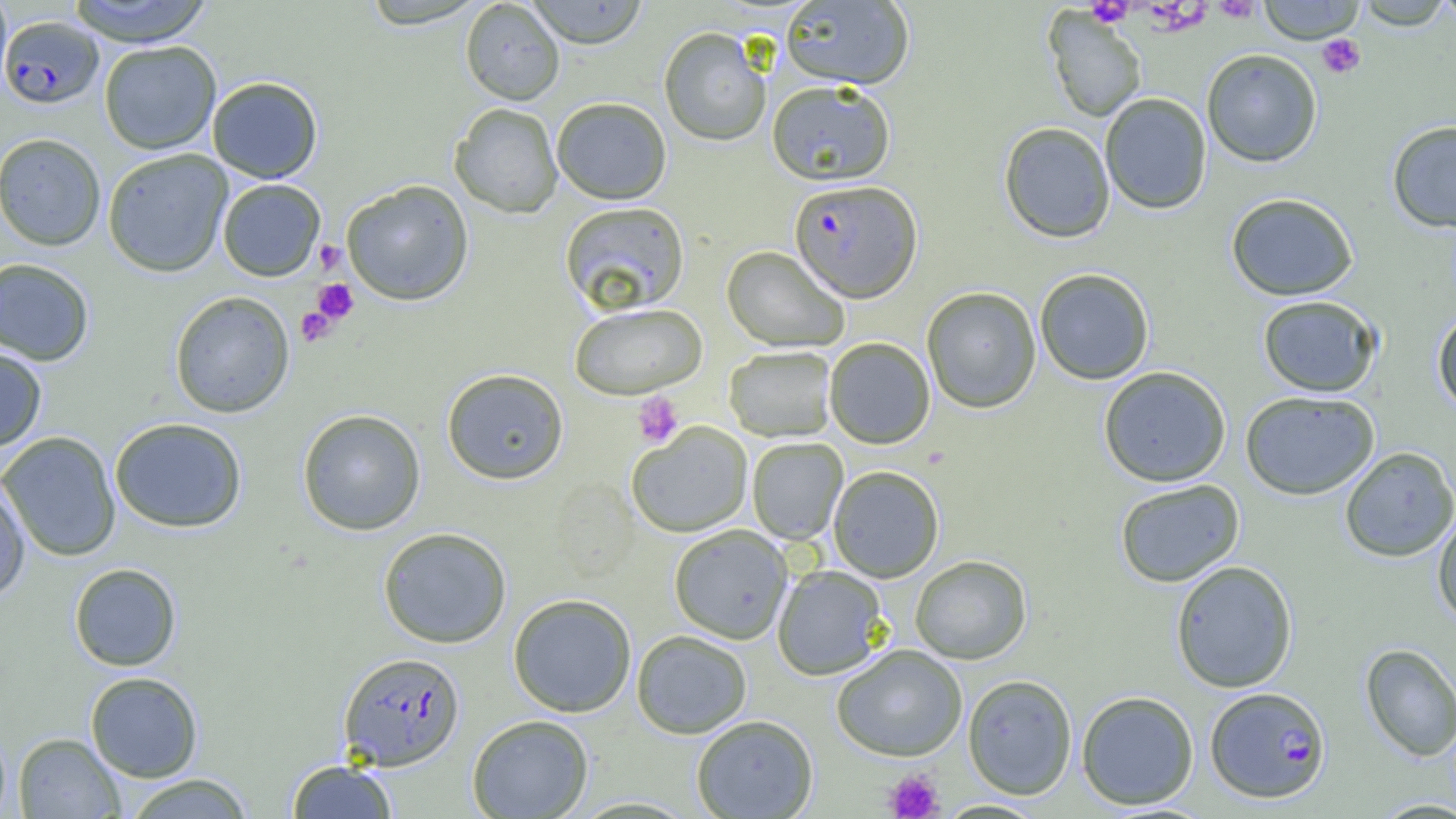

slide-level diagnosis = Plasmodium falciparum
platelet locations = approximate bounding boxes as [x1, y1, x2, y2] in pixels: [1211, 0, 1262, 23], [1086, 1, 1133, 27], [1317, 34, 1366, 78], [314, 240, 346, 274], [310, 279, 359, 326], [295, 305, 338, 347], [632, 392, 684, 448], [883, 768, 944, 818]
uninfected red blood cell locations = approximate bounding boxes as [x1, y1, x2, y2] in pixels: [0, 0, 13, 101], [64, 0, 216, 45], [357, 0, 489, 30], [460, 0, 565, 105], [526, 0, 649, 48], [1256, 0, 1366, 43], [1431, 0, 1456, 27], [781, 1, 914, 89], [1353, 2, 1456, 30], [1043, 10, 1147, 123], [659, 27, 771, 146], [99, 40, 222, 154], [1201, 49, 1323, 167], [207, 76, 323, 183], [766, 80, 896, 185], [1099, 93, 1212, 215], [551, 97, 672, 204], [449, 102, 564, 218], [1386, 120, 1456, 233], [998, 122, 1116, 243], [0, 132, 107, 251], [102, 149, 233, 277], [217, 179, 326, 281], [341, 179, 474, 306], [1225, 192, 1359, 301], [559, 201, 689, 316], [722, 245, 850, 352], [0, 257, 96, 366], [1034, 268, 1155, 385], [921, 286, 1042, 414], [169, 291, 295, 418], [1257, 295, 1382, 397], [569, 302, 707, 399], [1432, 310, 1456, 416], [824, 337, 936, 449], [0, 346, 48, 453], [723, 346, 837, 442], [1098, 366, 1232, 487], [441, 368, 569, 485], [1240, 391, 1380, 500], [297, 408, 426, 535], [109, 417, 247, 533], [626, 422, 753, 538], [0, 431, 121, 562], [746, 437, 848, 545], [1339, 446, 1456, 563], [828, 465, 944, 583], [0, 477, 31, 604], [1114, 479, 1245, 587], [1432, 510, 1456, 627], [668, 525, 793, 644], [377, 526, 512, 648], [909, 555, 1032, 664], [1170, 560, 1299, 693], [68, 563, 182, 671], [772, 565, 889, 680], [507, 593, 637, 717], [631, 630, 752, 739], [1360, 643, 1456, 762], [831, 644, 968, 761], [85, 671, 203, 783], [962, 674, 1078, 800], [1076, 690, 1199, 810], [467, 714, 594, 818], [691, 714, 819, 818], [0, 723, 11, 818], [13, 732, 125, 818], [286, 759, 398, 818], [122, 773, 255, 818]
image size = 1456×819 pixels
preparation = thin blood smear
magnification = 1000x
modality = optical microscopy
field of view = one of a larger specimen
Plasmodium falciparum-infected red blood cell locations = approximate bounding boxes as [x1, y1, x2, y2] in pixels: [1, 15, 103, 108], [789, 179, 922, 303], [338, 652, 465, 770], [1205, 686, 1331, 804]